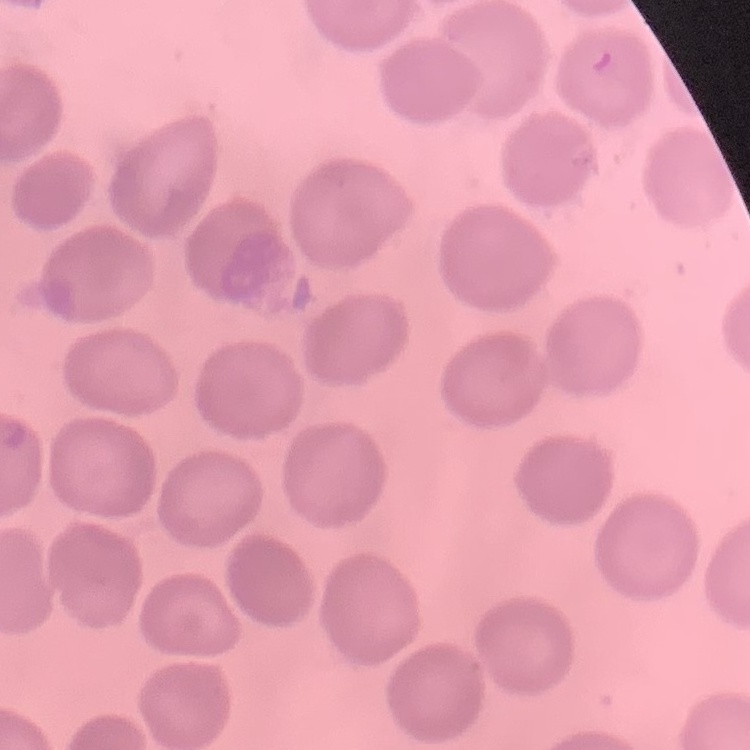
Summary:
  - Red blood cell morphology: no rouleaux formation
  - Preparation: thin blood film
  - Image type: square crop of a larger photomicrograph
  - Stain: Field's or Giemsa